Evaluate for malaria.
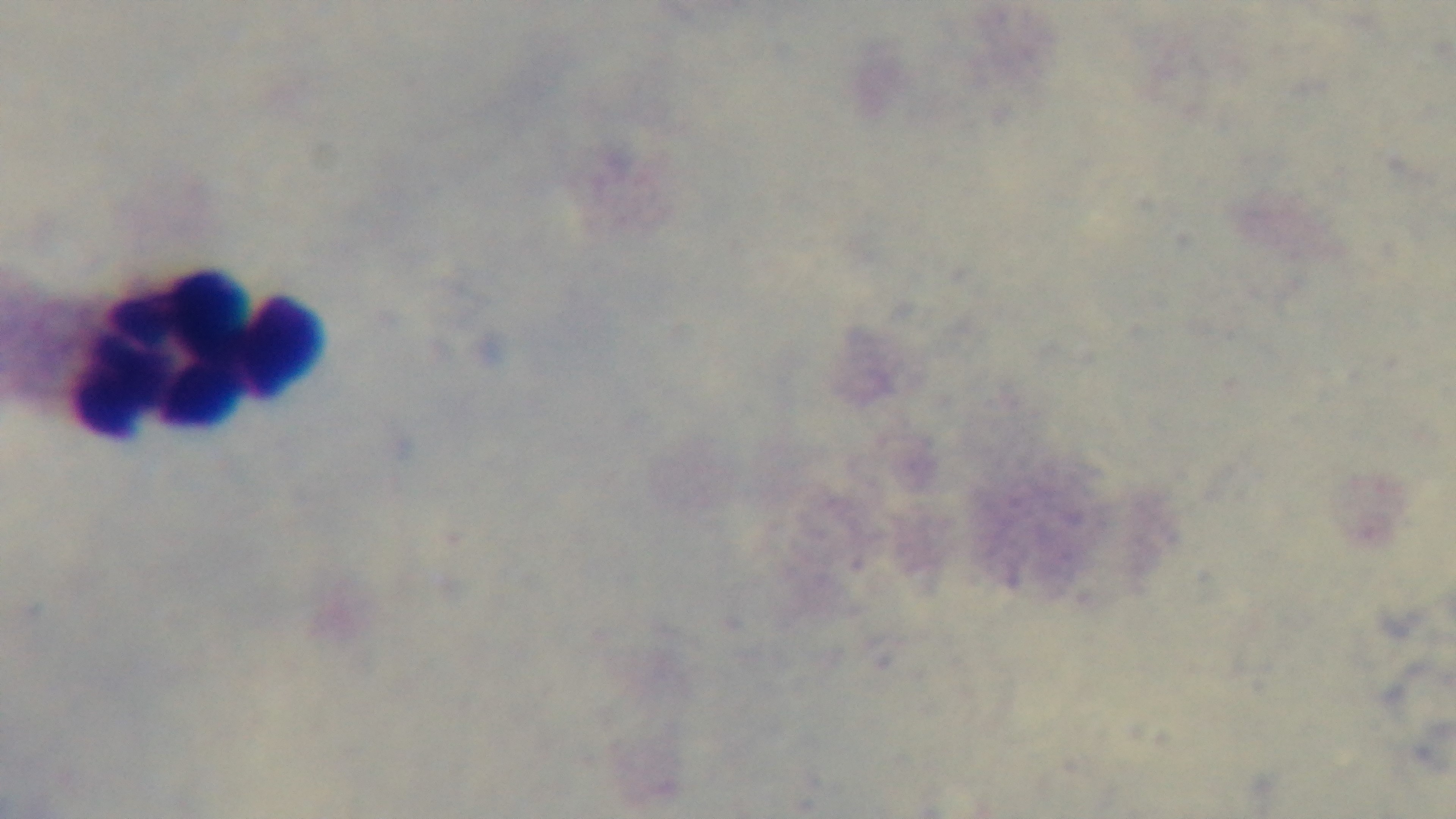

It is uninfected.

Single field of view. Captured with a mounted 4K digital camera. Giemsa stain. Photomicrograph. Preparation: thick blood film. Oil-immersion objective, 100x.